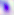

Captured at 400x magnification. Photomicrograph. Toxoplasma gondii is seen.